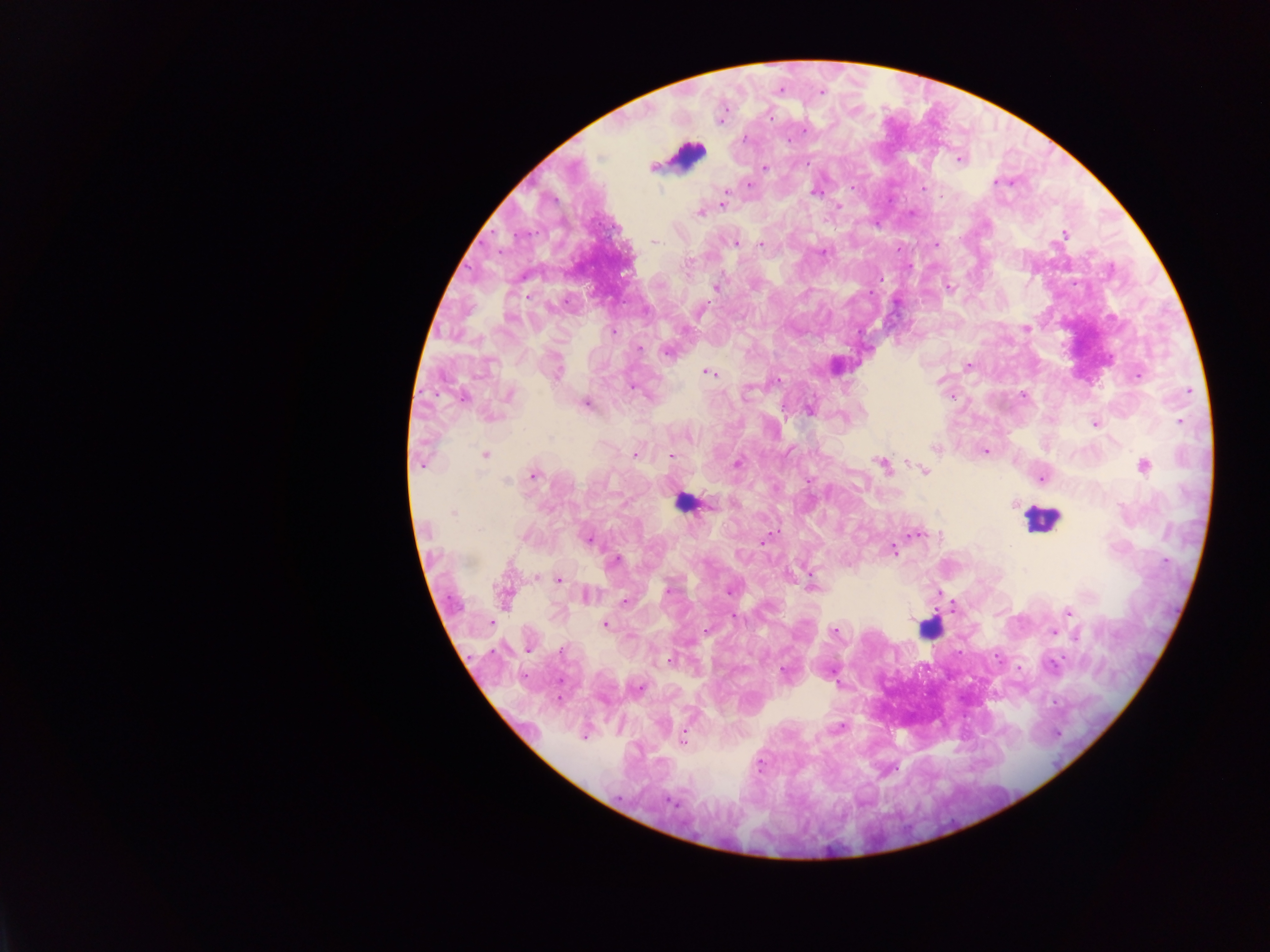
Approximate centers as x y in pixels.
Summary:
  - Leukocyte locations: 687 155; 685 502; 1040 519; 929 628
  - Malaria parasite locations: 779 90; 822 92; 805 130; 745 139; 788 141; 959 159; 807 163; 652 168; 765 168; 996 182; 749 184; 851 187; 923 188; 814 191; 725 193; 723 204; 839 207; 700 213; 1065 234; 655 242; 736 244; 760 244; 936 244; 823 252; 688 265; 716 287; 949 287; 870 292; 1026 328; 614 332; 640 350; 667 352; 967 366; 557 372; 709 373; 1138 376; 632 387; 1188 390; 1023 394; 509 395; 952 397; 462 398; 586 404; 808 410; 490 416; 1181 421; 1094 424; 688 437; 935 448; 986 452; 485 455; 635 455; 671 456; 737 463; 422 464; 881 464; 1143 465; 925 471; 534 476; 1042 479; 506 481; 809 481; 1015 505; 453 514; 479 529; 916 534; 589 540; 764 540; 893 550; 616 561; 1025 571; 536 577; 558 580; 812 585; 668 591; 729 591; 587 596; 505 597; 625 601; 1068 611; 734 618; 491 623; 606 624; 705 631; 835 632; 1054 632; 1077 635; 528 649; 562 649; 670 661; 1054 667; 1019 668; 783 671; 640 688; 585 737; 683 739; 671 801
  - Preparation: thick blood smear
  - Field of view: single
  - Image size: 1270×952 pixels
  - Country: Ghana
  - Capture: mobile-phone photograph through a microscope